State which parasite is depicted.
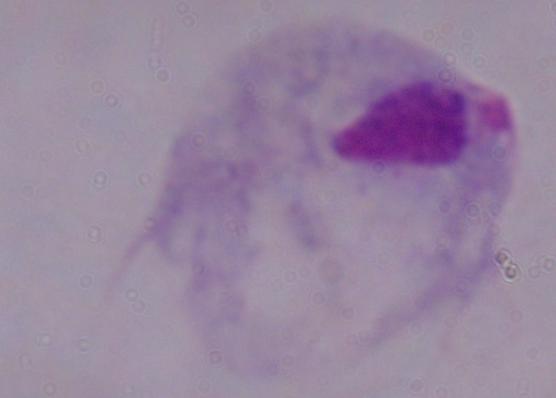
This is a trichomonad.

modality: micrograph
magnification: 1000x